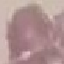

malaria status = uninfected
capture = smartphone camera at the microscope eyepiece
preparation = thin smear
stain = Giemsa
image type = automatically extracted cell patch, resized to 64 × 64 pixels